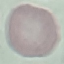

Malaria status: uninfected. Photographed with a smartphone camera at the microscope eyepiece. Cell patch, automatically extracted from a larger field of view and resized to 64 × 64 pixels. Giemsa-stained preparation. Thin blood film.